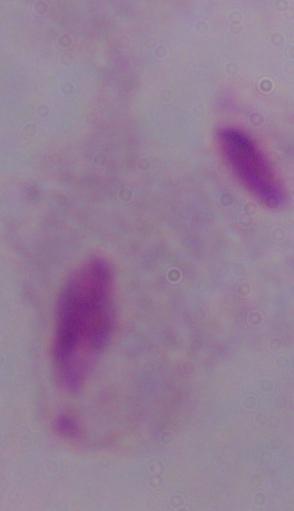
Micrograph. A trichomonad is seen. Captured at 1000x magnification.